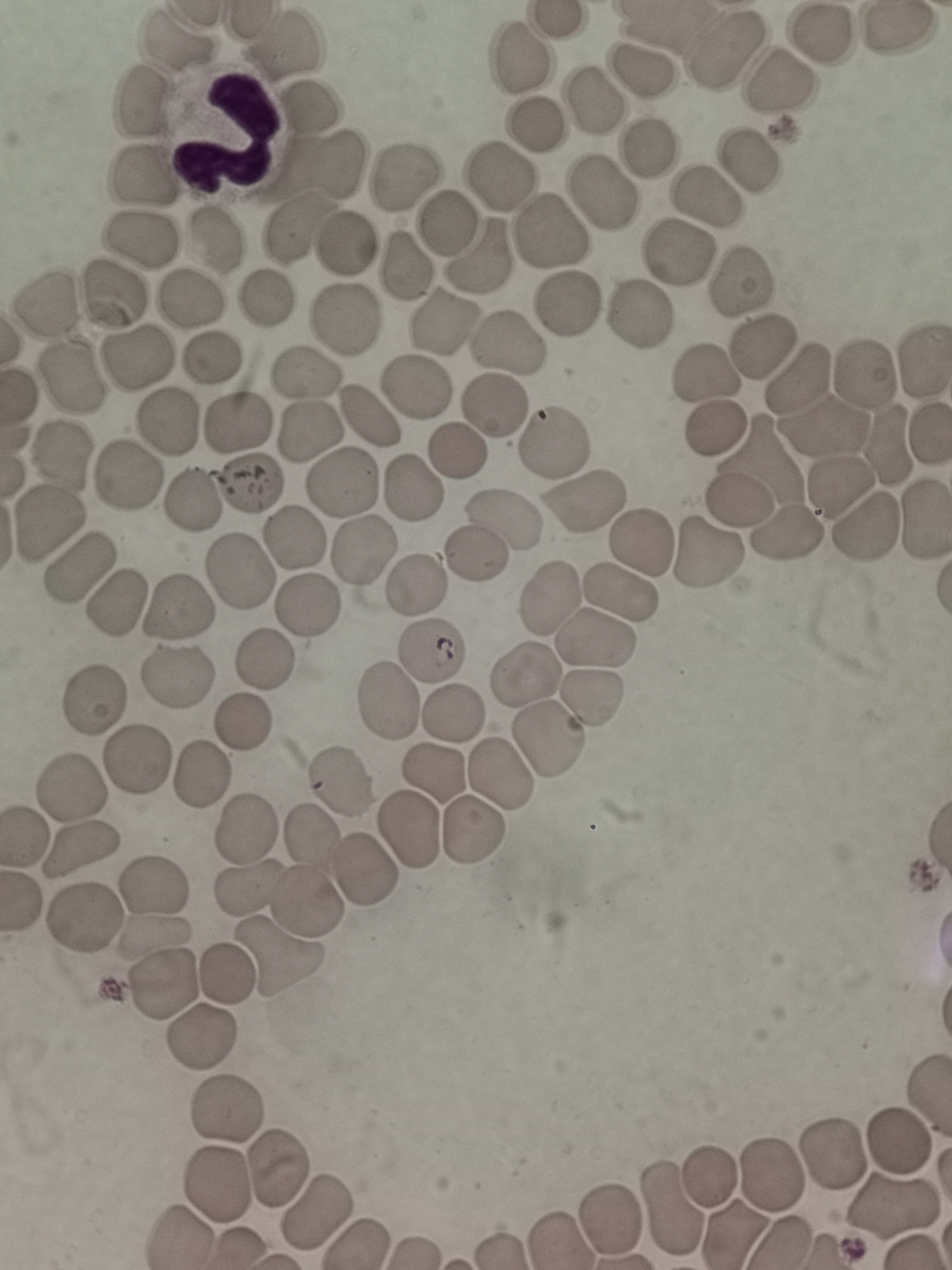
cell_locations: 'approximate centers as (x, y) in pixels: (816, 33), (174, 43), (283, 44), (727, 50), (524, 59), (639, 73), (781, 82), (593, 98), (145, 100), (311, 100), (536, 123), (651, 147), (337, 159), (747, 165), (402, 174), (504, 176), (139, 179), (603, 195), (707, 198), (445, 220), (302, 227), (551, 231), (206, 240), (140, 241), (346, 247), (676, 255), (480, 256), (404, 267), (739, 286), (112, 296), (566, 298), (263, 299), (182, 303), (51, 305), (638, 315), (339, 322), (442, 322), (506, 348), (762, 348), (214, 358), (141, 359), (709, 372), (69, 374), (864, 374), (306, 377), (802, 381), (415, 386), (490, 407), (367, 415), (169, 417), (237, 423), (825, 425), (719, 428), (304, 430), (555, 442), (886, 445), (455, 455), (761, 459), (59, 460), (126, 475), (343, 480), (244, 488), (412, 488), (839, 489), (586, 496), (191, 499), (740, 501), (502, 517), (54, 525), (860, 528), (298, 533), (782, 538), (640, 541), (366, 548), (477, 552), (705, 553), (78, 567), (243, 569), (417, 581), (621, 592), (551, 594), (310, 601), (116, 602), (174, 606), (597, 639), (429, 654), (261, 664), (175, 671), (532, 675), (593, 698), (390, 700), (92, 701), (454, 713), (242, 725), (549, 741), (139, 761), (500, 772), (438, 775), (202, 776), (74, 787), (335, 788), (245, 831), (406, 833), (471, 833), (314, 838), (85, 854), (366, 870), (152, 890), (245, 890), (306, 904), (81, 919), (157, 936), (279, 957), (224, 979), (163, 987), (203, 1034), (225, 1115), (903, 1143), (832, 1155), (275, 1168), (776, 1170), (712, 1176), (216, 1182), (892, 1204), (670, 1206), (315, 1211), (608, 1219)'
stain: Giemsa
image_size: 952×1270 pixels
field_of_view: single
capture: smartphone through the microscope eyepiece
preparation: thin blood smear